Report the malaria status of this cell.
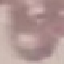
It is uninfected.

Giemsa-stained preparation. Thin blood film. Photographed with a smartphone camera at the microscope eyepiece. Automatically extracted cell patch, resized to 64 × 64 pixels.